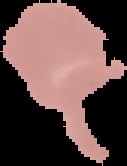 Image is 127×166 pixels. From a thin blood film. The area outside the segmented cell region is set to black. Malaria status: uninfected.